Give a bounding box for every leukocyte visible.
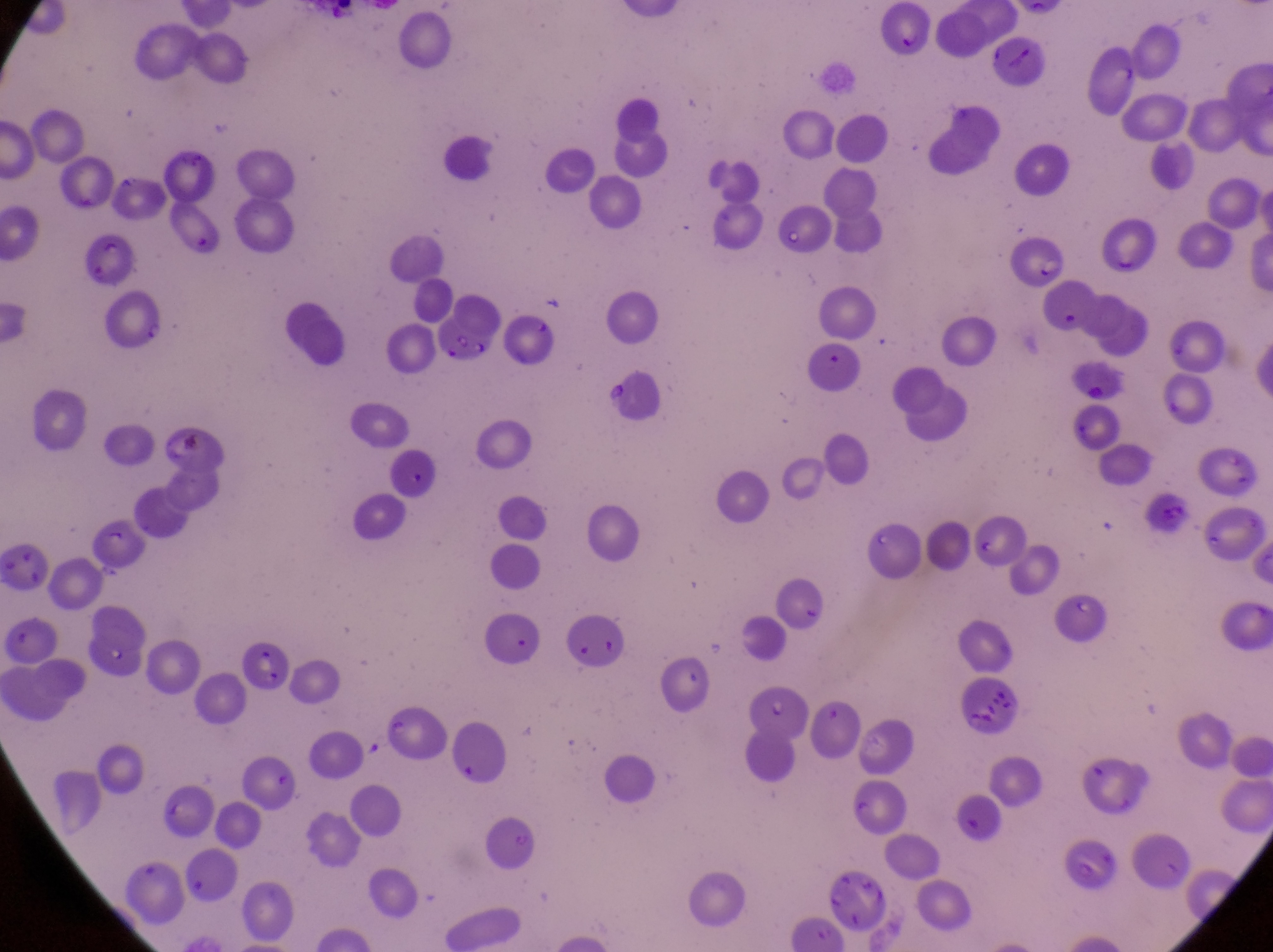

No leukocytes observed.

Approximate bounding boxes as (left, top, right, bottom) in pixels.
Summary:
  - Artifact (platelet-like body, stain precipitate, or debris) locations: (961, 687, 1023, 737)
  - Parasitised red blood cell locations: (1011, 229, 1064, 294), (70, 237, 133, 289), (99, 287, 174, 349), (237, 644, 295, 697)
  - Preparation: thin blood smear
  - Field of view: single
  - Magnification: 1000x
  - Country: Uganda
  - Capture: smartphone photograph through the eyepiece of an Olympus CX-23 microscope
  - Image size: 1273×952 pixels